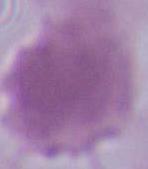
Summary:
  - Magnification: 1000x
  - Modality: photomicrograph
  - Identification: red blood cell